Locate every Plasmodium parasite.
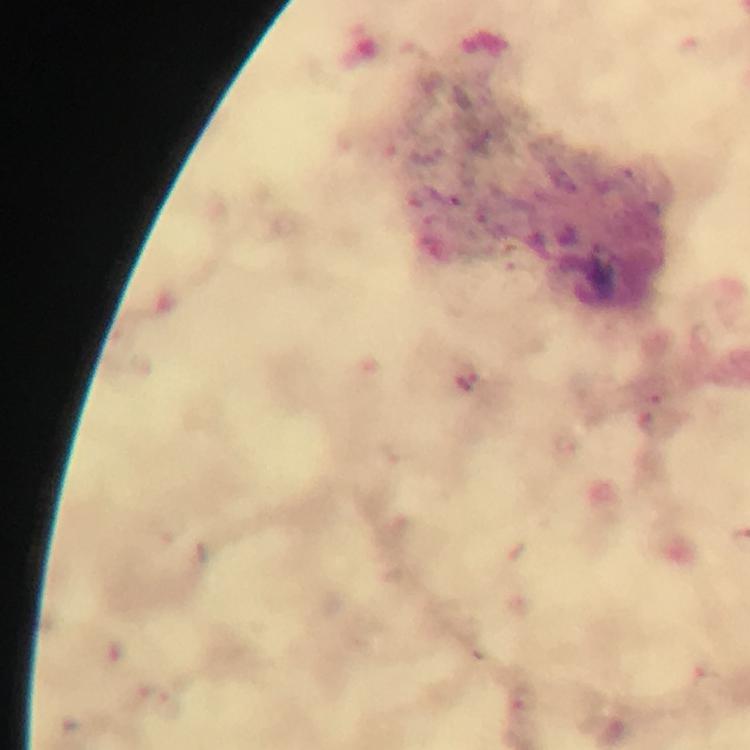

Approximate object centers, in pixels from the top-left corner.
Plasmodium parasites: (x=465, y=375), (x=524, y=702).

A crop from one field of view. Giemsa stain. Image is 750×750 pixels. From a diagnostic examination for malaria. 100x magnification. Thick smear. Immersion oil applied. Photographed with a smartphone mounted on the microscope.